Give the position of every leukocyte visible.
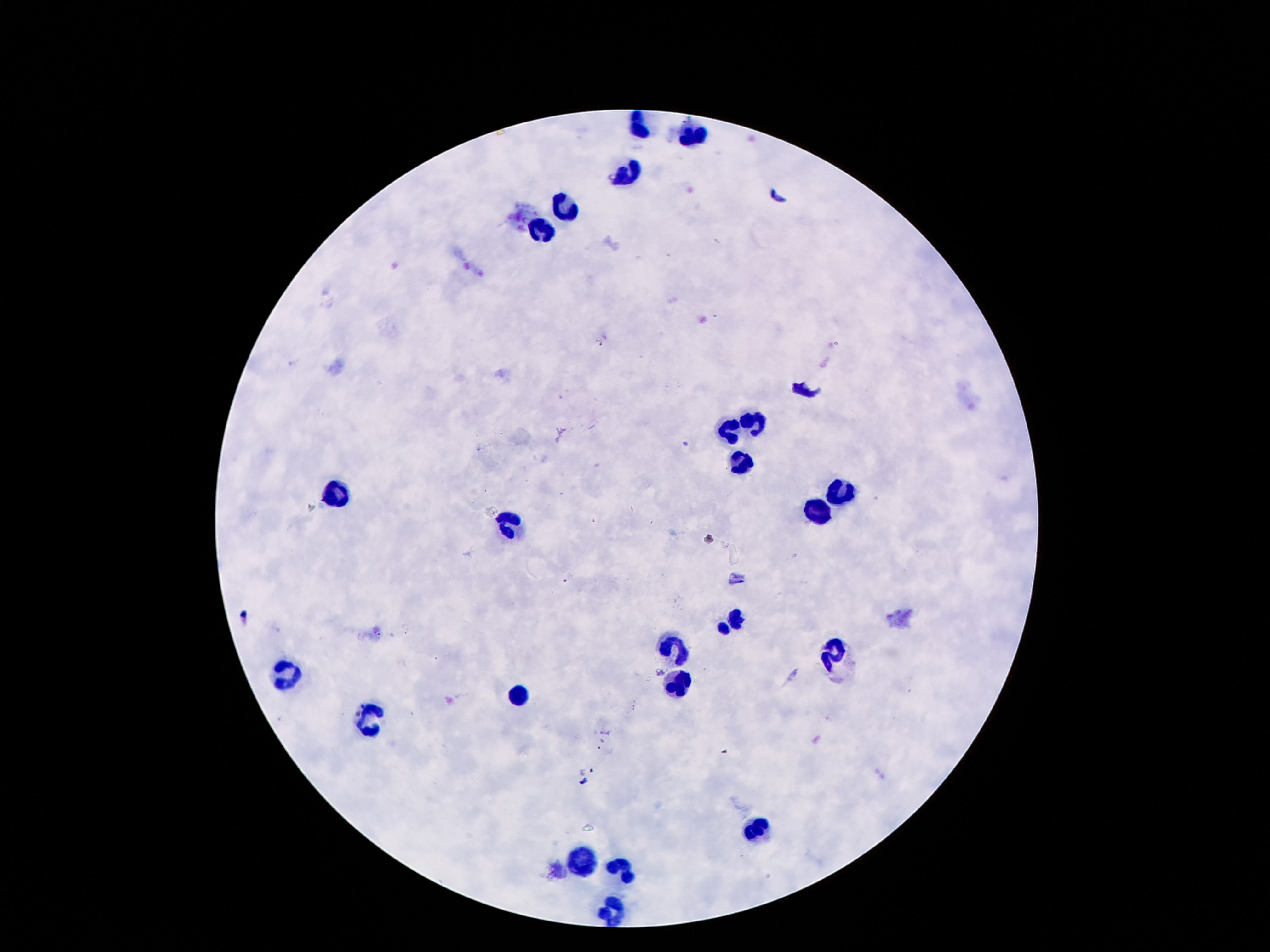
Approximate centers as (x, y) in pixels.
Leukocytes: (638, 126), (693, 133), (627, 172), (566, 207), (539, 231), (752, 425), (732, 430), (739, 462), (334, 495), (841, 495), (815, 514), (503, 522), (734, 618), (675, 643), (832, 652), (284, 672), (676, 688), (516, 695), (368, 718), (761, 827), (582, 864), (625, 868), (614, 908).

field of view = one from this slide
magnification = 100x
patient malaria status = not infected
image size = 1270×952 pixels
stain = Giemsa
capture = smartphone camera through the microscope eyepiece
preparation = thick blood film